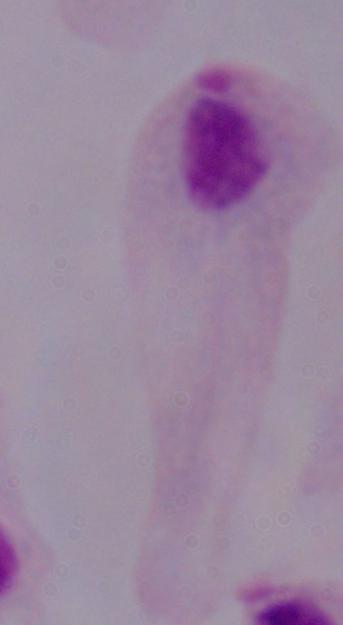
Summary:
  - Identification: trichomonad
  - Modality: micrograph
  - Magnification: 1000x